State the blood parasite species.
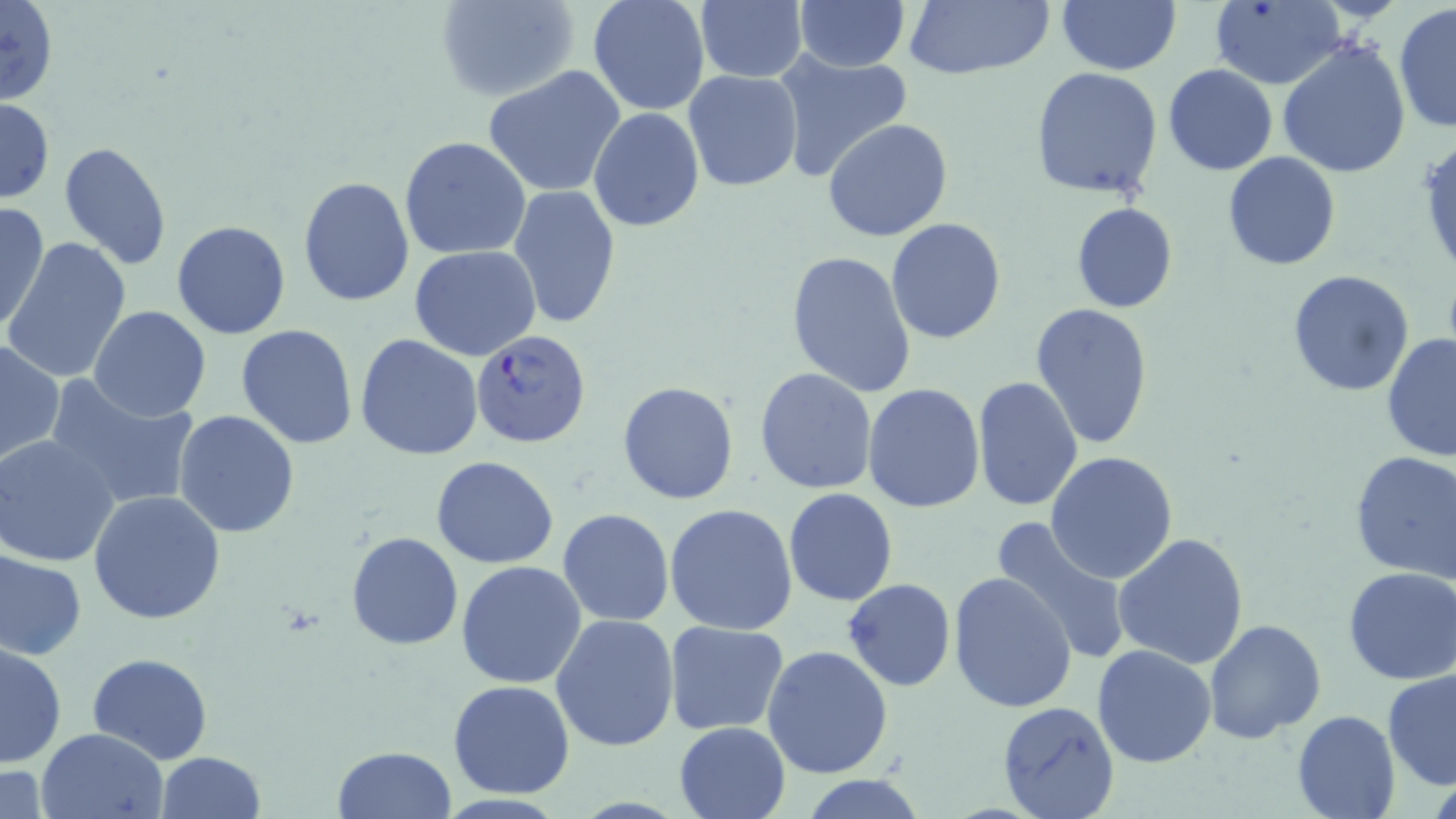
Plasmodium falciparum.

Summary:
  - Coordinate format: approximate bounding boxes as [x1, y1, x2, y2] in pixels
  - Plasmodium falciparum-infected red blood cell locations: [471, 329, 590, 449]
  - Uninfected red blood cell locations: [0, 0, 60, 108], [435, 0, 581, 103], [587, 0, 710, 115], [792, 0, 909, 71], [904, 0, 1054, 81], [1209, 0, 1346, 90], [1058, 1, 1180, 75], [695, 2, 807, 82], [1394, 4, 1456, 135], [1276, 36, 1411, 179], [772, 49, 913, 183], [1163, 64, 1278, 175], [1030, 66, 1164, 199], [483, 67, 626, 197], [683, 69, 802, 192], [0, 97, 53, 202], [589, 108, 705, 230], [824, 118, 952, 242], [400, 137, 531, 260], [58, 141, 173, 271], [1222, 152, 1341, 272], [297, 176, 416, 305], [509, 185, 623, 329], [0, 202, 49, 334], [1071, 203, 1177, 314], [885, 218, 1007, 344], [171, 221, 291, 339], [5, 239, 132, 382], [410, 245, 541, 361], [786, 250, 917, 402], [1286, 268, 1416, 398], [1029, 302, 1154, 453], [88, 306, 212, 422], [237, 325, 359, 449], [1381, 331, 1456, 462], [356, 334, 484, 460], [0, 340, 64, 465], [755, 368, 877, 495], [972, 375, 1083, 511], [48, 376, 202, 511], [617, 381, 738, 504], [862, 383, 986, 514], [174, 410, 301, 538], [0, 437, 122, 569], [1045, 451, 1178, 584], [1349, 451, 1456, 582], [432, 456, 560, 568], [784, 487, 897, 606], [87, 491, 228, 626], [665, 504, 798, 636], [557, 509, 673, 628], [987, 518, 1130, 665], [346, 530, 463, 652], [1113, 531, 1249, 670], [0, 549, 86, 659], [457, 560, 587, 688], [1343, 568, 1456, 684], [949, 572, 1078, 713], [843, 578, 956, 691], [551, 613, 680, 752], [1205, 619, 1327, 742], [662, 621, 790, 736], [0, 642, 66, 769], [762, 644, 892, 779], [1092, 644, 1218, 768], [86, 651, 214, 765], [1382, 668, 1456, 791], [447, 679, 575, 798], [996, 701, 1119, 819], [1291, 711, 1400, 819], [673, 721, 791, 819], [37, 728, 169, 819], [333, 745, 456, 818], [157, 751, 265, 819], [0, 759, 49, 819], [799, 777, 929, 818]
  - Field of view: single
  - Magnification: 1000x
  - Modality: light microscopy
  - Preparation: thin blood smear
  - Image size: 1456×819 pixels
  - Stain: May-Grünwald-Giemsa